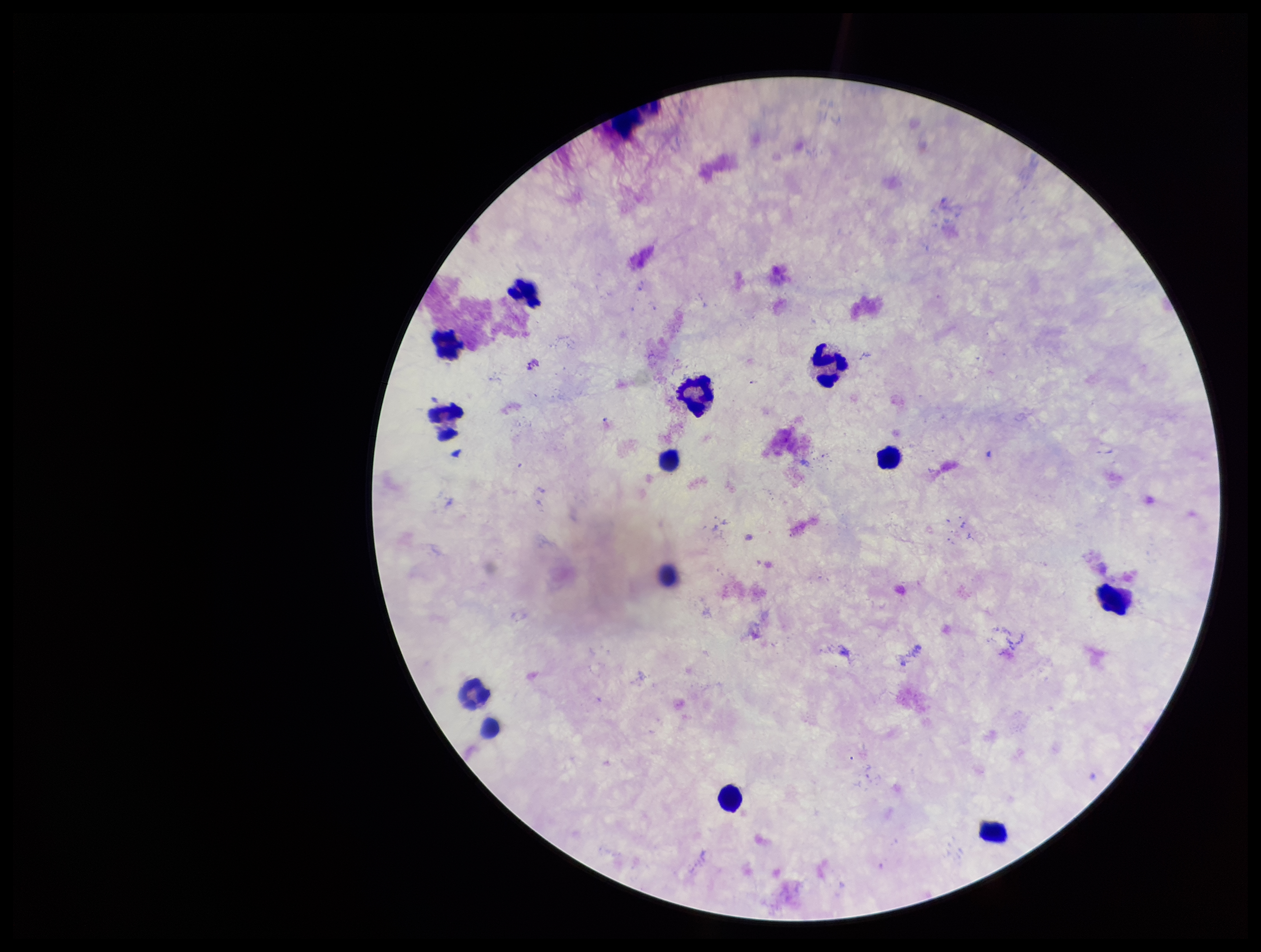
Preparation: thick. Image is 1261×952 pixels. One field from this slide. Parasite count: 0. Plasmodium parasites: none identified. Leukocyte count: 11. Giemsa stain. Patient malaria status: negative. Photographed through the microscope eyepiece with a smartphone camera.